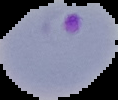

{
  "image_type": "segmented cell region with the area outside set to black",
  "image_size": "118×100 pixels",
  "preparation": "thin blood film",
  "result": "malaria parasites detected"
}